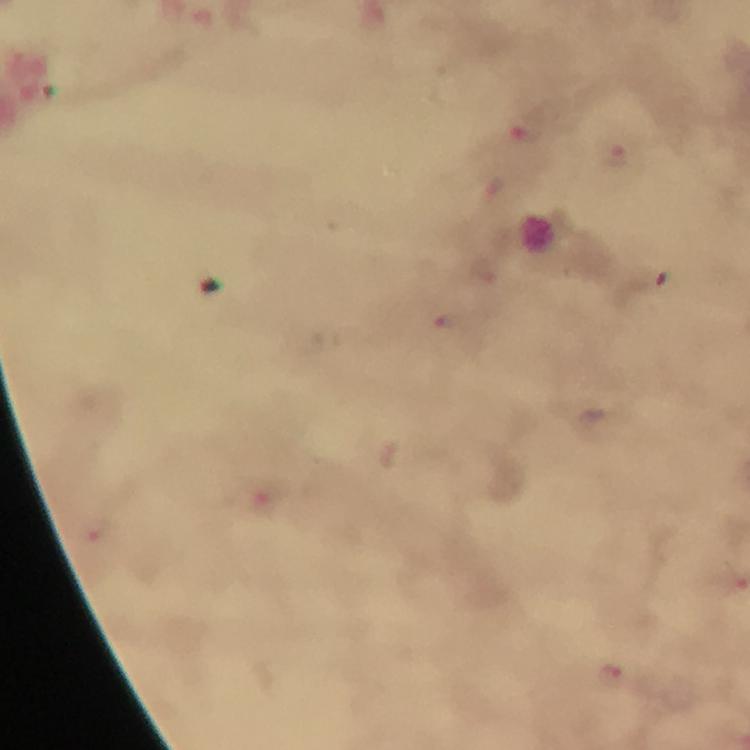

context: from a malaria diagnostic workup
cropped_from: a single field of view
image_size: 750×750 pixels
stain: Giemsa
magnification: 100x
immersion_oil: used
capture: smartphone camera through the microscope
preparation: thick smear
malaria_parasite_locations: 'approximate centers as [x, y] in pixels: [616, 155], [445, 321], [612, 675]'